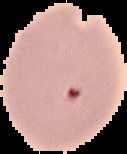

Segmented cell region on a black background. Result: malaria parasites detected. Image is 127×154 pixels. From a thin blood film.